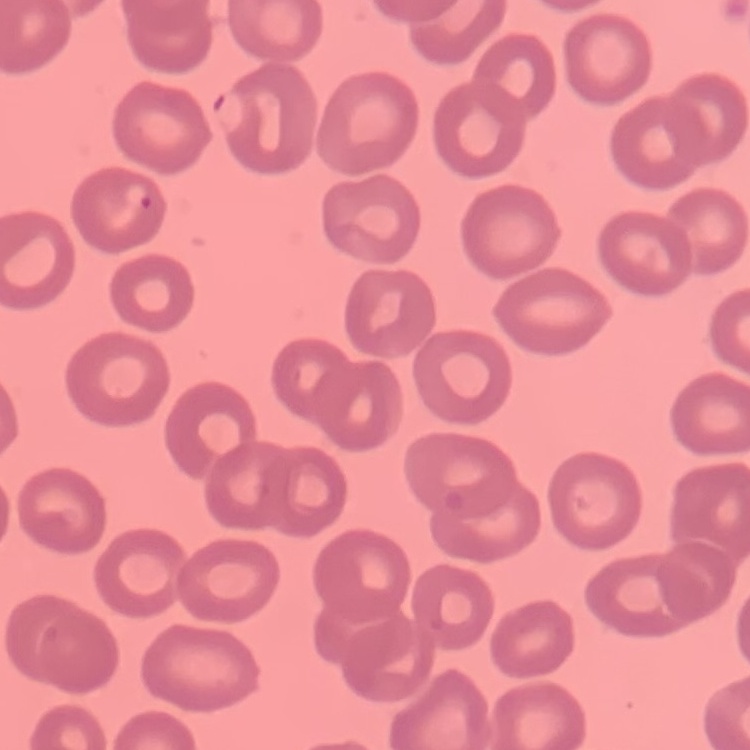

erythrocyte_morphology: no rouleaux formation
image_type: square crop of a larger photomicrograph
preparation: thin blood smear
stain: Field's or Giemsa